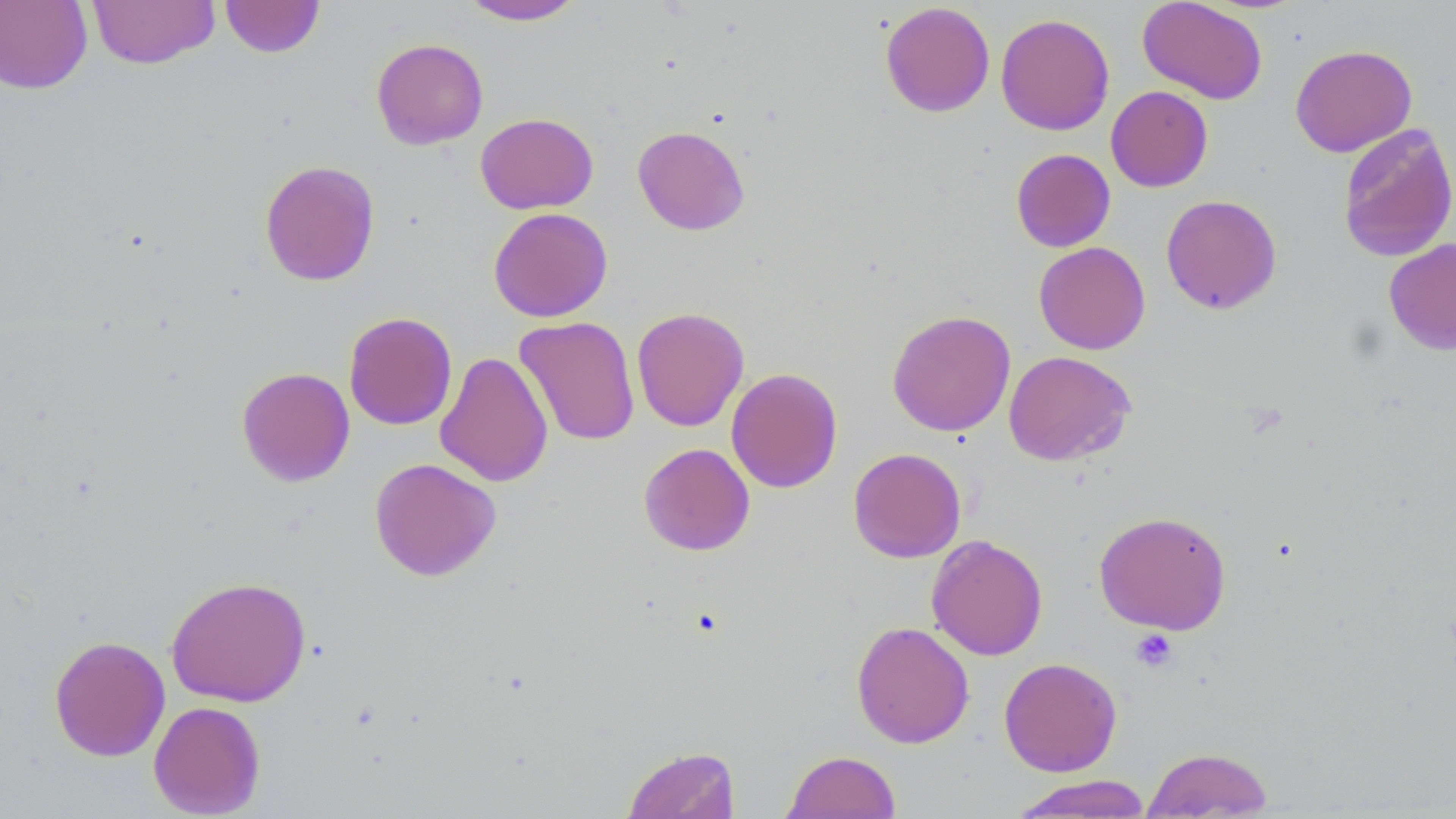
Approximate bounding boxes as (x1,y1)-(x2,y2) corner pairs in pixels. Uninfected red blood cell locations: (86,0)-(220,69), (219,0)-(325,58), (459,0)-(586,25), (1137,0)-(1268,104), (0,1)-(93,94), (879,2)-(995,117), (995,13)-(1115,135), (371,38)-(489,150), (1290,44)-(1417,157), (1106,86)-(1213,192), (475,112)-(599,214), (1337,123)-(1456,263), (632,125)-(750,235), (1011,148)-(1116,252), (259,159)-(381,286), (1161,194)-(1282,314), (488,207)-(613,323), (1384,239)-(1456,355), (1033,241)-(1151,354), (631,306)-(749,432), (887,309)-(1016,437), (343,312)-(457,430), (514,316)-(640,446), (435,351)-(554,488), (1003,351)-(1136,466), (236,367)-(355,487), (726,367)-(843,493), (638,442)-(755,556), (848,447)-(966,563), (369,457)-(501,581), (1094,511)-(1232,634), (926,534)-(1048,660), (165,575)-(312,707), (851,621)-(975,749), (48,635)-(170,762), (998,657)-(1122,777), (148,700)-(266,818), (622,745)-(740,819), (1142,746)-(1274,818), (781,750)-(902,818), (1008,774)-(1154,817). Platelet locations: (1130,629)-(1178,672). Slide-level diagnosis: negative for blood parasites. Image is 1456×819 pixels. 1000x magnification. Optical microscopy. Single field of view. May-Grünwald-Giemsa stain. Thin blood smear.